Give the extent of all uninfected red blood cells.
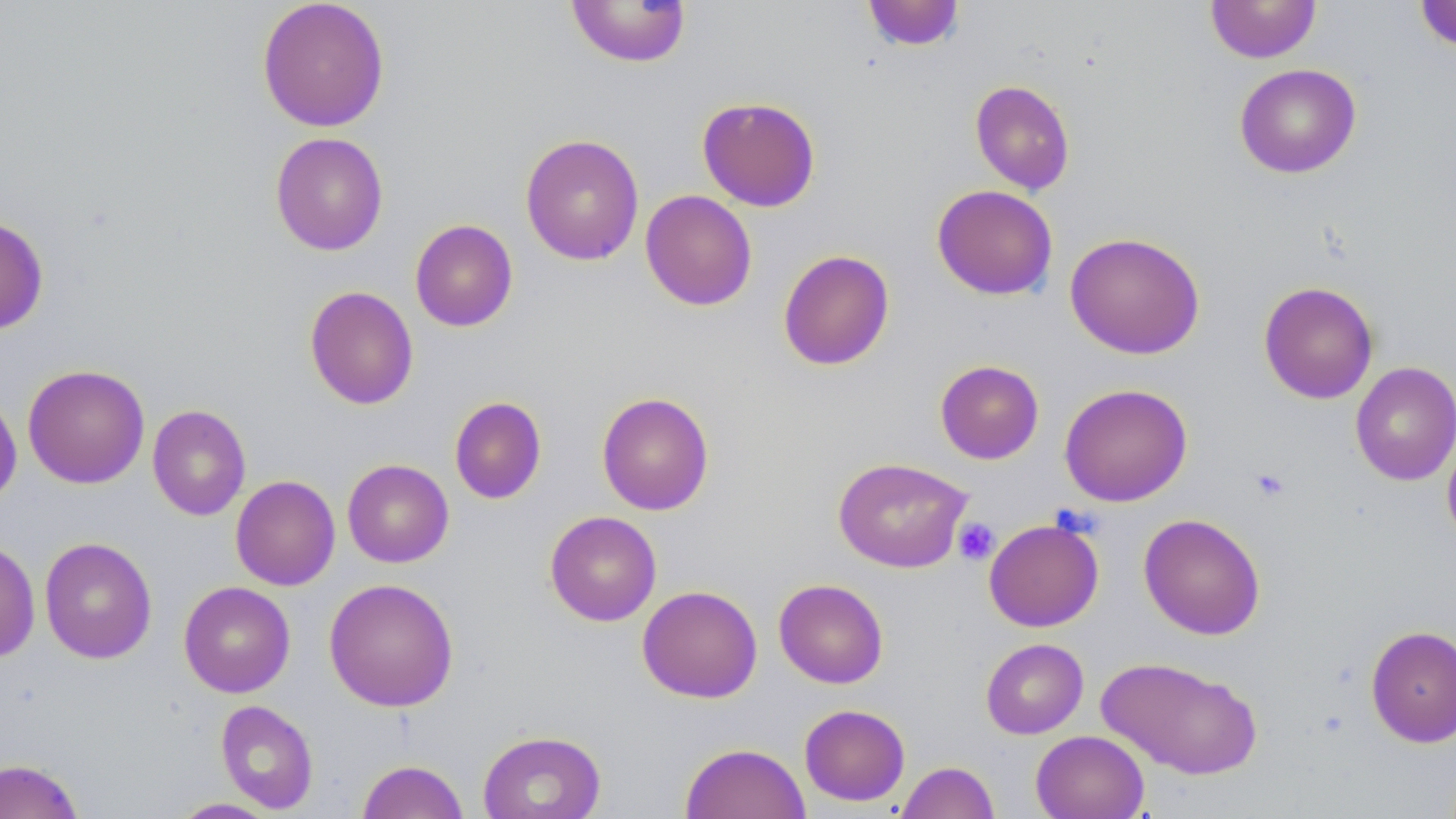
Approximate bounding boxes as (x1, y1, x2, y2) in pixels.
Uninfected red blood cells: (256, 0, 391, 132), (566, 0, 692, 67), (1205, 0, 1321, 63), (862, 1, 965, 52), (1413, 1, 1456, 53), (1234, 63, 1362, 178), (969, 79, 1076, 194), (696, 96, 821, 212), (270, 131, 389, 256), (519, 133, 645, 266), (932, 184, 1058, 300), (640, 190, 758, 311), (0, 213, 49, 335), (410, 219, 518, 332), (1064, 231, 1205, 359), (777, 249, 895, 371), (1258, 281, 1379, 404), (304, 286, 419, 409), (934, 359, 1044, 464), (1350, 360, 1456, 486), (22, 363, 150, 489), (1059, 383, 1193, 507), (596, 391, 715, 516), (0, 392, 22, 508), (449, 396, 547, 504), (147, 404, 251, 521), (1442, 432, 1456, 548), (832, 457, 974, 572), (342, 459, 454, 567), (230, 475, 340, 591), (544, 510, 662, 626), (1139, 513, 1266, 640), (983, 518, 1104, 632), (39, 537, 157, 664), (0, 539, 40, 663), (324, 577, 459, 712), (773, 578, 888, 688), (178, 581, 295, 698), (637, 585, 762, 703), (1365, 624, 1456, 748), (980, 638, 1089, 739), (1095, 656, 1263, 780), (215, 699, 319, 813), (799, 704, 911, 806), (477, 729, 606, 819), (1030, 730, 1149, 819), (679, 742, 811, 819), (0, 758, 84, 818), (356, 759, 468, 819), (896, 761, 1000, 819), (168, 797, 281, 818).

slide-level diagnosis = negative for blood parasites
field of view = single
magnification = 1000x
preparation = thin blood smear
image size = 1456×819 pixels
modality = optical microscopy
platelet locations = approximate bounding boxes as (x1, y1, x2, y2) in pixels: (1250, 468, 1290, 503), (954, 518, 999, 565)
stain = May-Grünwald-Giemsa